Locate every Plasmodium parasite.
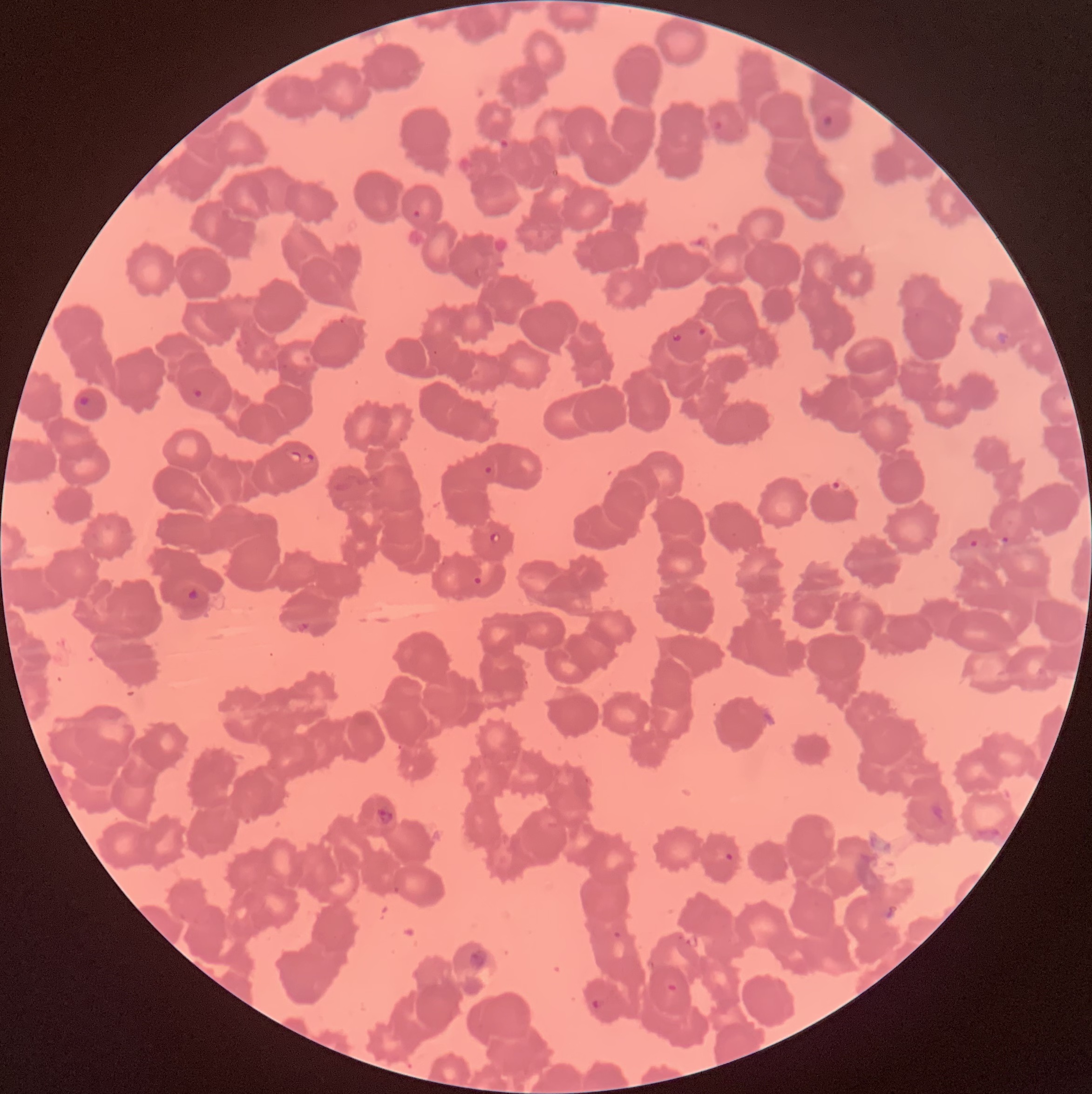

Approximate bounding boxes as named x1/y1/x2/y2 corners in pixels.
Plasmodium parasites: (x1=711, y1=113, x2=729, y2=131), (x1=821, y1=114, x2=834, y2=127), (x1=488, y1=137, x2=509, y2=154), (x1=412, y1=209, x2=422, y2=219), (x1=338, y1=318, x2=346, y2=324), (x1=696, y1=327, x2=708, y2=338), (x1=671, y1=332, x2=683, y2=343), (x1=431, y1=349, x2=440, y2=356), (x1=192, y1=386, x2=203, y2=399), (x1=78, y1=395, x2=91, y2=408), (x1=286, y1=449, x2=302, y2=463), (x1=303, y1=452, x2=315, y2=465), (x1=483, y1=465, x2=493, y2=476), (x1=825, y1=479, x2=847, y2=494), (x1=488, y1=532, x2=501, y2=545), (x1=1000, y1=535, x2=1011, y2=545), (x1=968, y1=538, x2=980, y2=549), (x1=472, y1=576, x2=483, y2=586), (x1=185, y1=587, x2=201, y2=603), (x1=297, y1=621, x2=310, y2=634), (x1=929, y1=800, x2=946, y2=824), (x1=376, y1=807, x2=394, y2=826), (x1=975, y1=825, x2=1001, y2=844), (x1=724, y1=852, x2=734, y2=862), (x1=392, y1=885, x2=401, y2=895), (x1=883, y1=903, x2=901, y2=922), (x1=613, y1=931, x2=623, y2=941), (x1=468, y1=949, x2=487, y2=970), (x1=666, y1=983, x2=678, y2=993), (x1=590, y1=998, x2=603, y2=1010).

Summary:
  - Preparation: thin blood film
  - Modality: light microscopy
  - Red blood cell morphology: rouleaux formation
  - Image size: 1092×1094 pixels